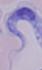
Summary:
  - Modality: photomicrograph
  - Magnification: 1000x
  - Identification: trypanosome